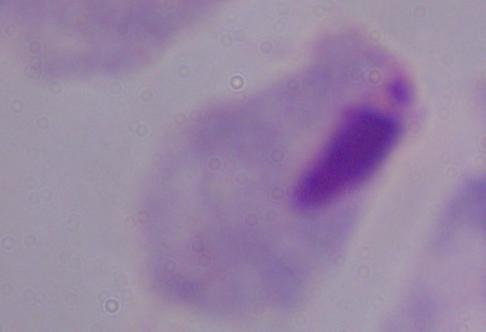

identification = trichomonad
magnification = 1000x
modality = photomicrograph